Locate every blood parasite and identify its species.
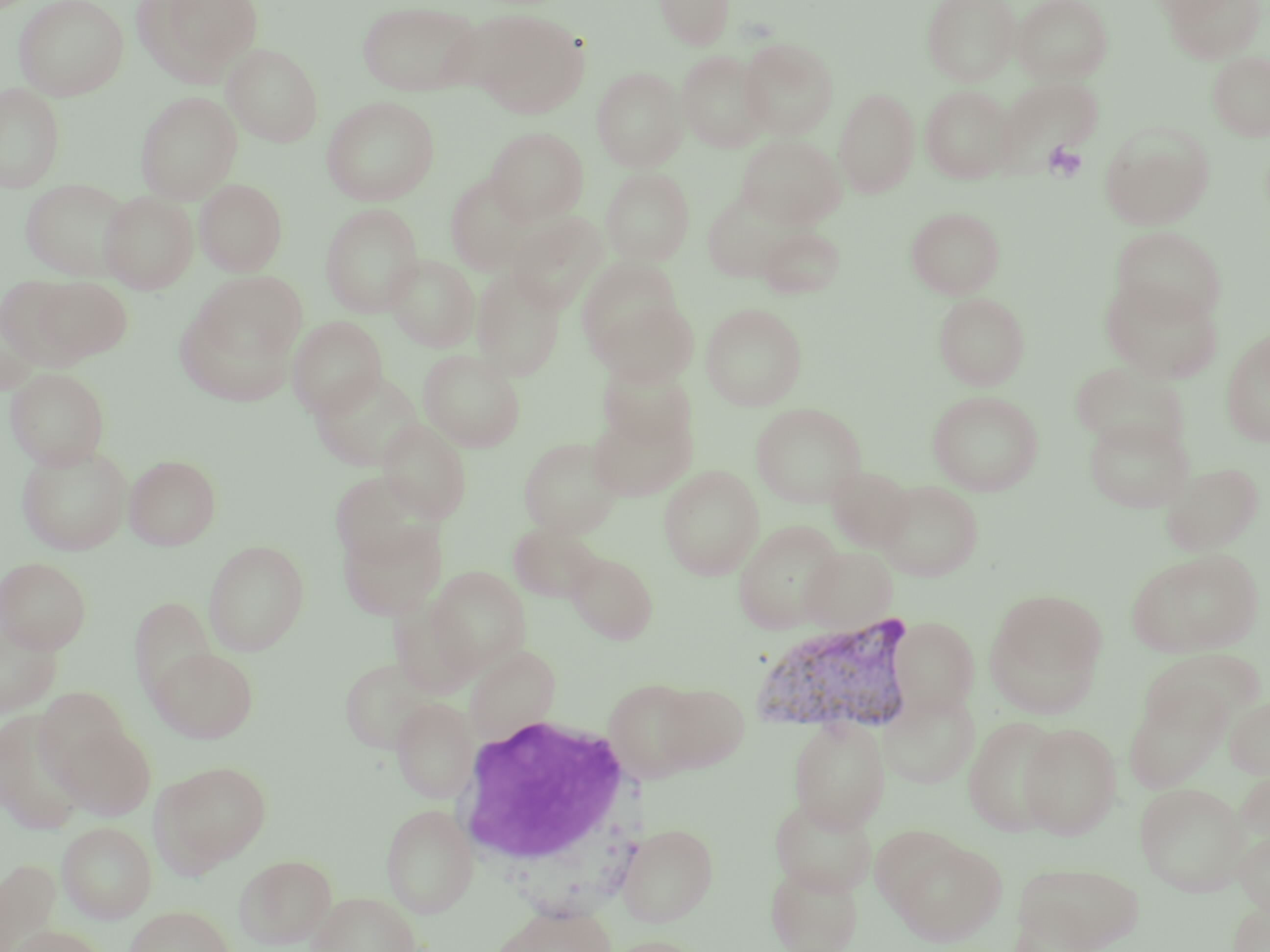

Approximate bounding boxes as named x1/y1/x2/y2 corners in pixels.
Plasmodium vivax-infected red blood cells: (x1=751, y1=614, x2=919, y2=740).
No Plasmodium falciparum, Plasmodium ovale, Plasmodium malariae, Babesia divergens, or Trypanosoma brucei observed.

Platelet locations: (x1=1042, y1=141, x2=1087, y2=183). Uninfected red blood cell locations: (x1=14, y1=0, x2=129, y2=101), (x1=133, y1=0, x2=264, y2=86), (x1=654, y1=0, x2=734, y2=49), (x1=922, y1=0, x2=1021, y2=86), (x1=1013, y1=0, x2=1112, y2=84), (x1=1149, y1=0, x2=1237, y2=22), (x1=1165, y1=0, x2=1264, y2=63), (x1=357, y1=1, x2=484, y2=97), (x1=470, y1=10, x2=589, y2=117), (x1=738, y1=38, x2=838, y2=139), (x1=223, y1=43, x2=323, y2=146), (x1=676, y1=50, x2=772, y2=153), (x1=1208, y1=51, x2=1270, y2=141), (x1=592, y1=67, x2=687, y2=171), (x1=994, y1=76, x2=1102, y2=170), (x1=0, y1=83, x2=65, y2=192), (x1=920, y1=84, x2=1016, y2=183), (x1=834, y1=87, x2=920, y2=198), (x1=135, y1=91, x2=242, y2=204), (x1=321, y1=96, x2=440, y2=206), (x1=1100, y1=122, x2=1213, y2=229), (x1=486, y1=127, x2=588, y2=225), (x1=737, y1=135, x2=845, y2=228), (x1=600, y1=167, x2=695, y2=266), (x1=444, y1=173, x2=541, y2=275), (x1=20, y1=178, x2=132, y2=280), (x1=195, y1=178, x2=287, y2=276), (x1=100, y1=190, x2=198, y2=294), (x1=703, y1=194, x2=790, y2=283), (x1=321, y1=204, x2=423, y2=317), (x1=906, y1=207, x2=1004, y2=299), (x1=507, y1=212, x2=608, y2=313), (x1=757, y1=226, x2=846, y2=298), (x1=1111, y1=226, x2=1226, y2=326), (x1=384, y1=254, x2=480, y2=352), (x1=578, y1=258, x2=686, y2=365), (x1=471, y1=267, x2=565, y2=381), (x1=193, y1=271, x2=308, y2=369), (x1=29, y1=276, x2=133, y2=363), (x1=1101, y1=276, x2=1224, y2=383), (x1=0, y1=281, x2=79, y2=385), (x1=934, y1=292, x2=1030, y2=390), (x1=593, y1=294, x2=698, y2=386), (x1=170, y1=299, x2=302, y2=409), (x1=1, y1=302, x2=43, y2=396), (x1=701, y1=303, x2=807, y2=410), (x1=287, y1=316, x2=387, y2=418), (x1=1221, y1=328, x2=1270, y2=448), (x1=418, y1=350, x2=525, y2=452), (x1=597, y1=362, x2=696, y2=450), (x1=5, y1=367, x2=110, y2=470), (x1=310, y1=369, x2=425, y2=471), (x1=928, y1=390, x2=1043, y2=495), (x1=751, y1=403, x2=867, y2=508), (x1=587, y1=405, x2=695, y2=501), (x1=1083, y1=414, x2=1195, y2=513), (x1=377, y1=418, x2=472, y2=522), (x1=518, y1=437, x2=624, y2=538), (x1=17, y1=443, x2=133, y2=555), (x1=124, y1=454, x2=221, y2=550), (x1=1161, y1=461, x2=1265, y2=555), (x1=658, y1=464, x2=763, y2=580), (x1=825, y1=465, x2=914, y2=552), (x1=330, y1=472, x2=437, y2=567), (x1=876, y1=480, x2=983, y2=581), (x1=337, y1=519, x2=447, y2=620), (x1=733, y1=520, x2=846, y2=633), (x1=509, y1=522, x2=604, y2=603), (x1=203, y1=540, x2=309, y2=655), (x1=800, y1=545, x2=899, y2=632), (x1=1128, y1=549, x2=1264, y2=657), (x1=567, y1=552, x2=657, y2=643), (x1=0, y1=557, x2=92, y2=654), (x1=425, y1=566, x2=531, y2=677), (x1=987, y1=589, x2=1107, y2=704), (x1=129, y1=597, x2=218, y2=704), (x1=0, y1=612, x2=62, y2=717), (x1=890, y1=618, x2=979, y2=716), (x1=465, y1=644, x2=561, y2=743), (x1=148, y1=646, x2=259, y2=743), (x1=1141, y1=651, x2=1264, y2=738), (x1=339, y1=657, x2=440, y2=754), (x1=603, y1=679, x2=702, y2=783), (x1=654, y1=682, x2=750, y2=771), (x1=1123, y1=685, x2=1231, y2=793), (x1=35, y1=687, x2=131, y2=784), (x1=879, y1=689, x2=979, y2=789), (x1=1225, y1=695, x2=1270, y2=779), (x1=391, y1=697, x2=479, y2=803), (x1=0, y1=709, x2=88, y2=835), (x1=963, y1=715, x2=1066, y2=836), (x1=789, y1=717, x2=889, y2=833), (x1=54, y1=721, x2=155, y2=820), (x1=1018, y1=722, x2=1122, y2=839), (x1=153, y1=760, x2=273, y2=874), (x1=1233, y1=763, x2=1270, y2=853), (x1=1135, y1=782, x2=1250, y2=896), (x1=769, y1=795, x2=877, y2=896), (x1=381, y1=803, x2=478, y2=918), (x1=57, y1=821, x2=157, y2=923), (x1=617, y1=822, x2=718, y2=926), (x1=1233, y1=827, x2=1270, y2=920), (x1=887, y1=836, x2=1007, y2=946), (x1=234, y1=854, x2=337, y2=949), (x1=0, y1=858, x2=61, y2=951), (x1=1011, y1=861, x2=1143, y2=951), (x1=766, y1=863, x2=863, y2=952), (x1=307, y1=891, x2=424, y2=952), (x1=1227, y1=896, x2=1270, y2=952), (x1=491, y1=902, x2=618, y2=952), (x1=124, y1=905, x2=235, y2=952), (x1=7, y1=925, x2=105, y2=952), (x1=600, y1=935, x2=712, y2=952). White blood cell locations: (x1=450, y1=714, x2=640, y2=872). Slide-level diagnosis: Plasmodium vivax. Thin blood film. May-Grünwald-Giemsa stain. 1000x magnification. Image is 1270×952 pixels. One field of a larger specimen. Light microscopy.